Comment on the morphology of the red blood cells.
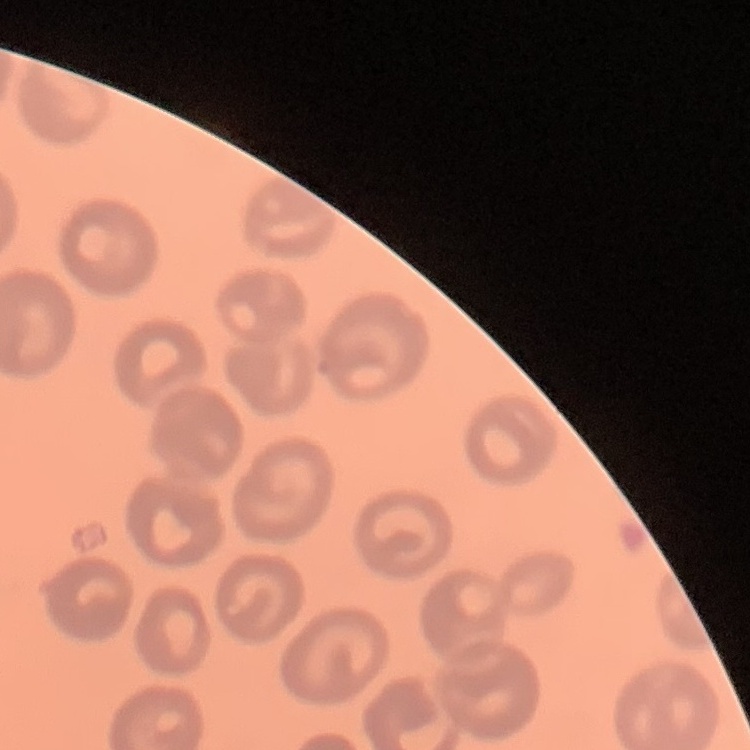
No rouleaux formation.

Field's or Giemsa stain. Thin blood smear. Square crop of a larger photomicrograph.